Identify the parasite.
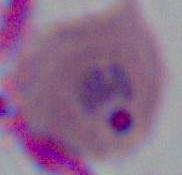

Plasmodium.

Summary:
  - Modality: micrograph
  - Magnification: 400x or 1000x